Give the position of every malaria parasite.
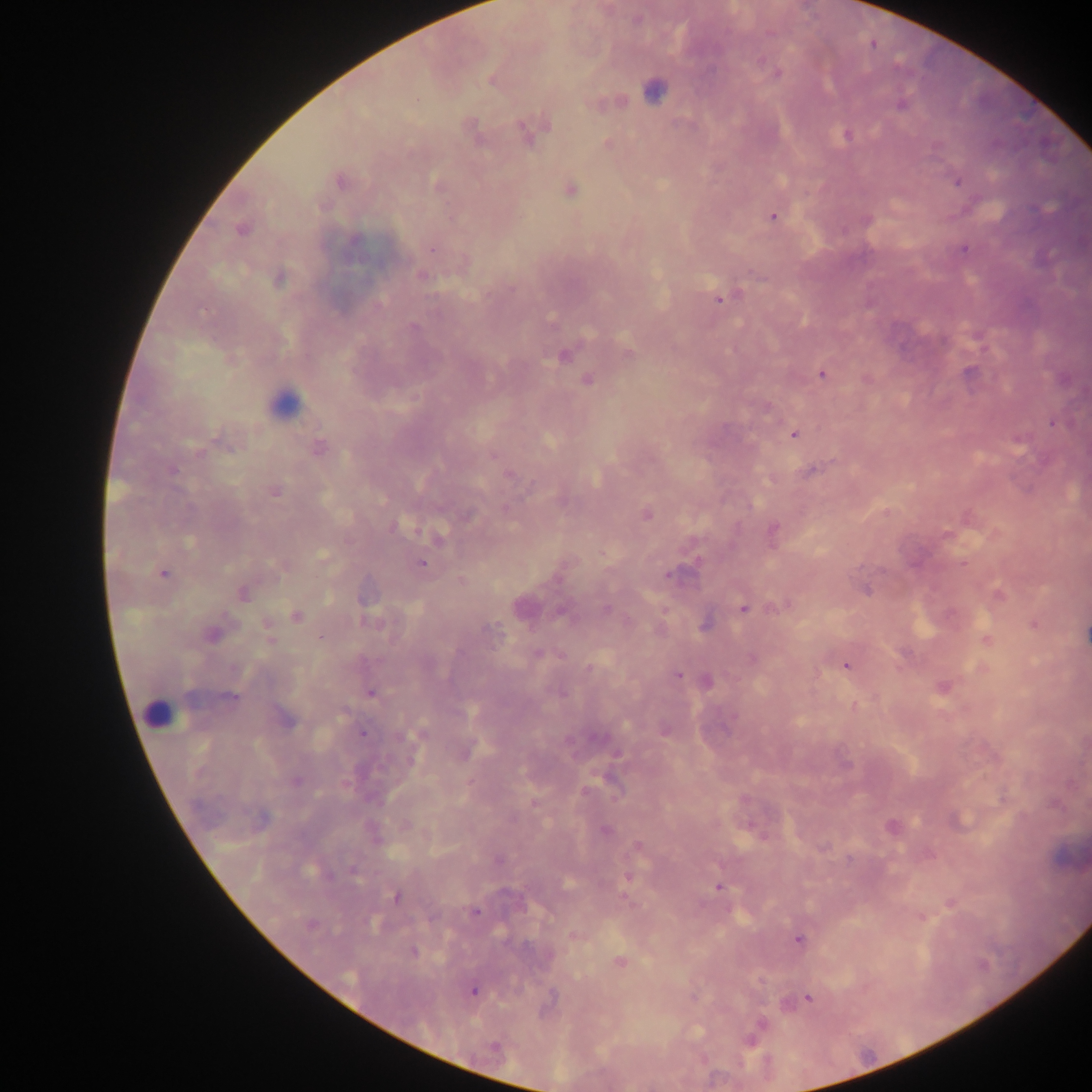
Approximate centers as (x, y) in pixels.
Malaria parasites: (762, 60), (778, 74), (520, 127), (844, 134), (937, 145), (339, 181), (959, 182), (772, 217), (431, 249), (963, 249), (421, 274), (511, 288), (719, 300), (822, 374), (587, 379), (767, 405), (1051, 422), (794, 433), (217, 435), (1016, 438), (320, 447), (199, 453), (173, 471), (509, 475), (275, 492), (421, 564), (164, 574), (667, 575), (868, 590), (243, 593), (743, 608), (295, 617), (364, 620), (266, 624), (1033, 624), (495, 626), (320, 637), (270, 640), (846, 663), (588, 667), (678, 675), (564, 693), (372, 694), (232, 699), (362, 733), (614, 755), (409, 760), (296, 782), (533, 803), (352, 870), (718, 887), (395, 897), (949, 902), (474, 911), (920, 918), (797, 939), (413, 951), (759, 980), (473, 991), (809, 998), (761, 1022), (751, 1043).

image_size: 1092×1092 pixels
capture: mobile-phone photograph through a microscope
country: Ghana
field_of_view: single
leukocyte_locations: 'approximate centers as (x, y) in pixels: (654, 92), (289, 398), (163, 711)'
preparation: thick blood smear